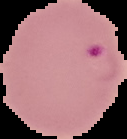 Malaria status: parasitized. Image is 127×139 pixels. The area outside the segmented cell region is set to black. From a thin blood smear.